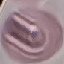

malaria status = uninfected
capture = smartphone camera at the microscope eyepiece
stain = Giemsa
image type = automatically extracted cell patch, resized to 64 × 64 pixels
preparation = thin blood smear